Report the malaria status of this cell.
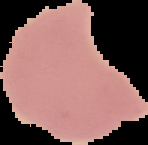

It is uninfected.

The area outside the segmented cell region is set to black. Image is 148×145 pixels. From a thin blood smear.